Classify this cell by malaria status.
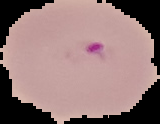
It is parasitized.

Image is 160×124 pixels. Segmented cell region on a black background. From a thin blood smear.